Outline each uninfected red blood cell.
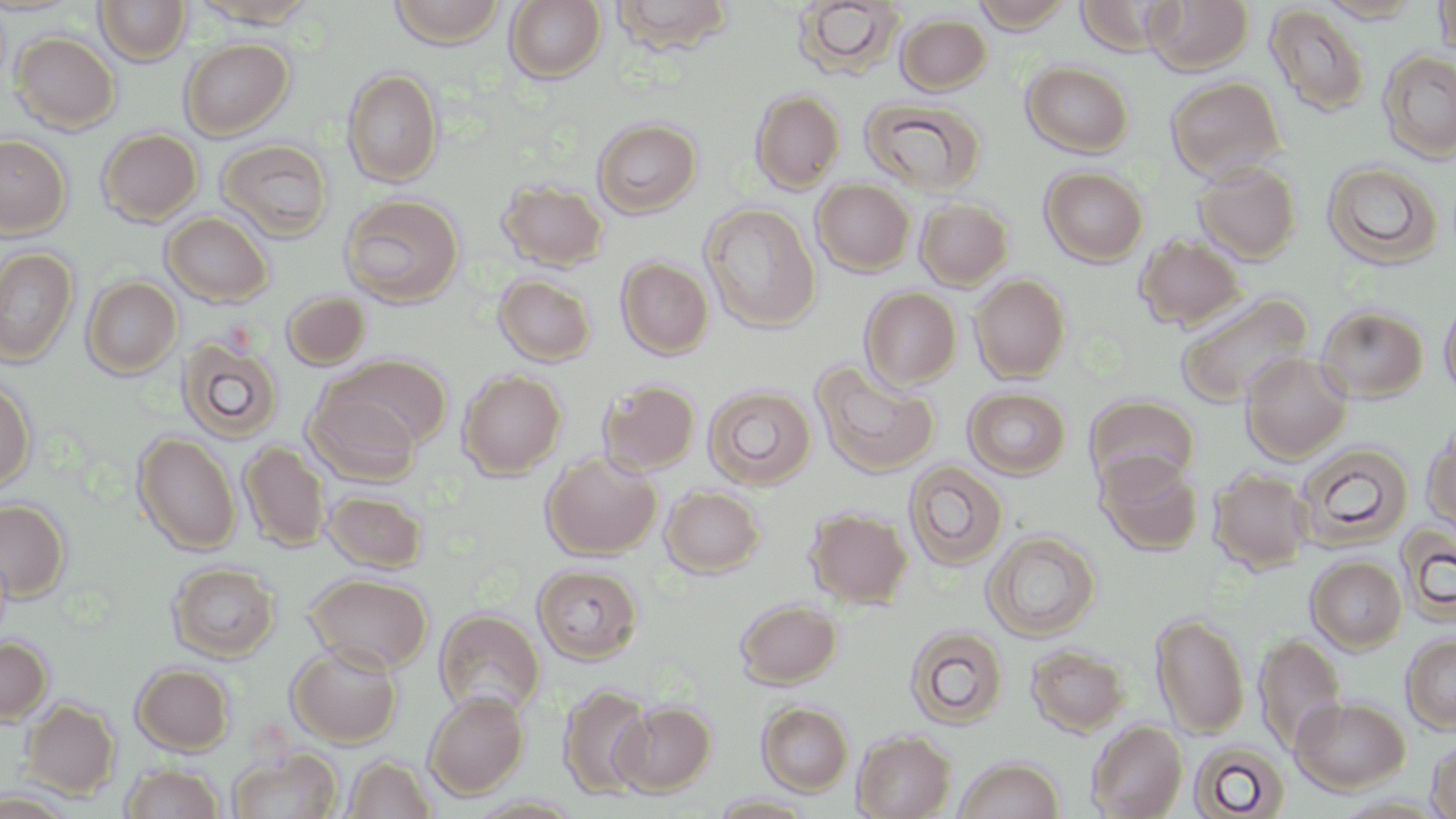

Approximate bounding boxes as (x1, y1, x2, y2) in pixels.
Uninfected red blood cells: (94, 0, 191, 65), (189, 0, 319, 28), (388, 0, 508, 48), (607, 0, 735, 54), (971, 0, 1073, 32), (1074, 0, 1179, 55), (1145, 0, 1254, 75), (1432, 0, 1456, 58), (504, 1, 607, 83), (792, 1, 906, 79), (1316, 1, 1426, 23), (1265, 4, 1370, 116), (895, 13, 991, 95), (10, 32, 121, 134), (179, 38, 294, 139), (1377, 50, 1456, 162), (1022, 61, 1133, 156), (342, 67, 444, 187), (1165, 75, 1286, 180), (750, 90, 844, 193), (859, 96, 987, 196), (593, 118, 702, 218), (97, 128, 202, 225), (0, 134, 71, 237), (217, 140, 335, 241), (1193, 159, 1302, 263), (1322, 161, 1443, 270), (1040, 166, 1148, 266), (812, 179, 915, 276), (497, 180, 609, 271), (339, 193, 465, 307), (915, 197, 1014, 289), (700, 203, 821, 332), (161, 212, 273, 306), (1135, 234, 1246, 331), (1, 247, 78, 366), (616, 257, 713, 359), (494, 274, 596, 366), (970, 274, 1071, 383), (82, 276, 182, 379), (860, 287, 961, 390), (281, 291, 371, 369), (1175, 292, 1313, 409), (1440, 294, 1456, 400), (1317, 305, 1428, 402), (176, 338, 284, 443), (1241, 353, 1351, 463), (331, 354, 452, 451), (811, 361, 940, 477), (458, 369, 566, 478), (0, 377, 36, 494), (597, 379, 701, 475), (703, 384, 816, 489), (964, 387, 1071, 479), (304, 388, 421, 485), (1085, 394, 1199, 492), (1422, 421, 1456, 537), (133, 431, 241, 555), (240, 441, 331, 552), (1296, 442, 1414, 551), (541, 451, 661, 559), (1097, 452, 1203, 556), (903, 460, 1009, 571), (1209, 468, 1312, 572), (661, 486, 765, 577), (324, 489, 427, 572), (0, 498, 71, 602), (805, 506, 912, 608), (1395, 522, 1456, 625), (983, 530, 1100, 641), (1306, 555, 1406, 652), (167, 562, 280, 661), (532, 563, 642, 663), (305, 573, 433, 673), (736, 599, 841, 687), (434, 609, 545, 716), (1151, 612, 1250, 738), (904, 624, 1009, 729), (1255, 633, 1346, 753), (1401, 633, 1456, 733), (0, 635, 52, 726), (287, 643, 403, 747), (1026, 643, 1129, 736), (131, 663, 234, 755), (558, 684, 656, 799), (423, 690, 530, 799), (1290, 694, 1411, 793), (20, 698, 120, 800), (613, 701, 715, 795), (758, 702, 854, 795), (1087, 720, 1187, 819), (853, 730, 955, 819), (1426, 736, 1456, 819), (1189, 741, 1290, 819), (228, 747, 342, 818), (341, 754, 437, 818), (953, 756, 1064, 819), (120, 762, 224, 819), (0, 790, 77, 818), (708, 792, 817, 818).

{
  "slide_level_diagnosis": "negative for blood parasites",
  "field_of_view": "single",
  "preparation": "thin blood smear",
  "modality": "light microscopy",
  "stain": "May-Grünwald-Giemsa",
  "image_size": "1456×819 pixels",
  "magnification": "1000x"
}